Classify this cell by malaria status.
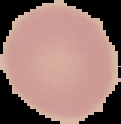
It is uninfected.

Summary:
  - Image type: segmented cell region on a black background
  - Image size: 121×124 pixels
  - Preparation: thin blood film